Assess the morphology of the red blood cells.
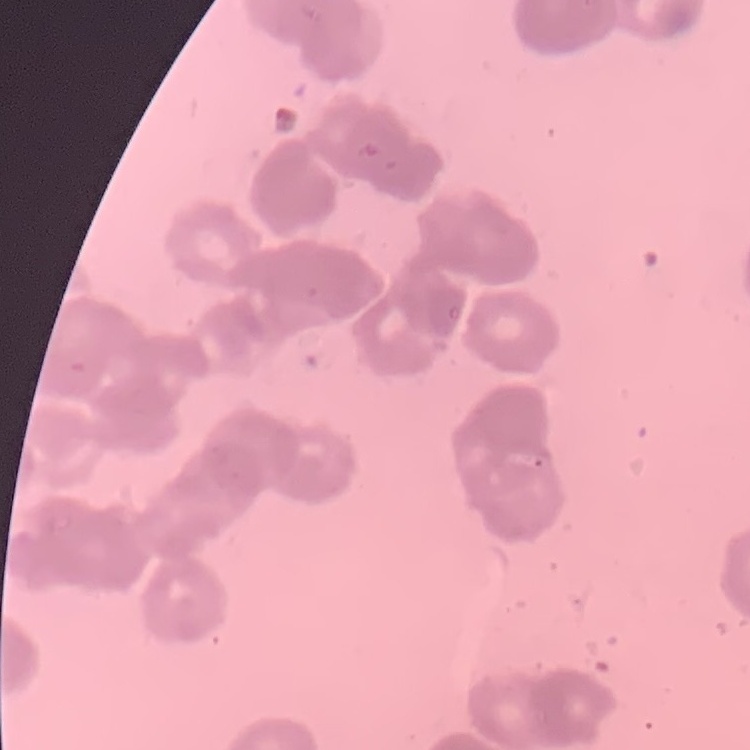
They show rouleaux formation.

Summary:
  - Preparation: thin peripheral smear
  - Stain: Field's or Giemsa
  - Image type: square crop of a larger photomicrograph